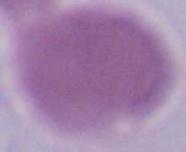

modality = photomicrograph
magnification = 1000x
identification = erythrocyte